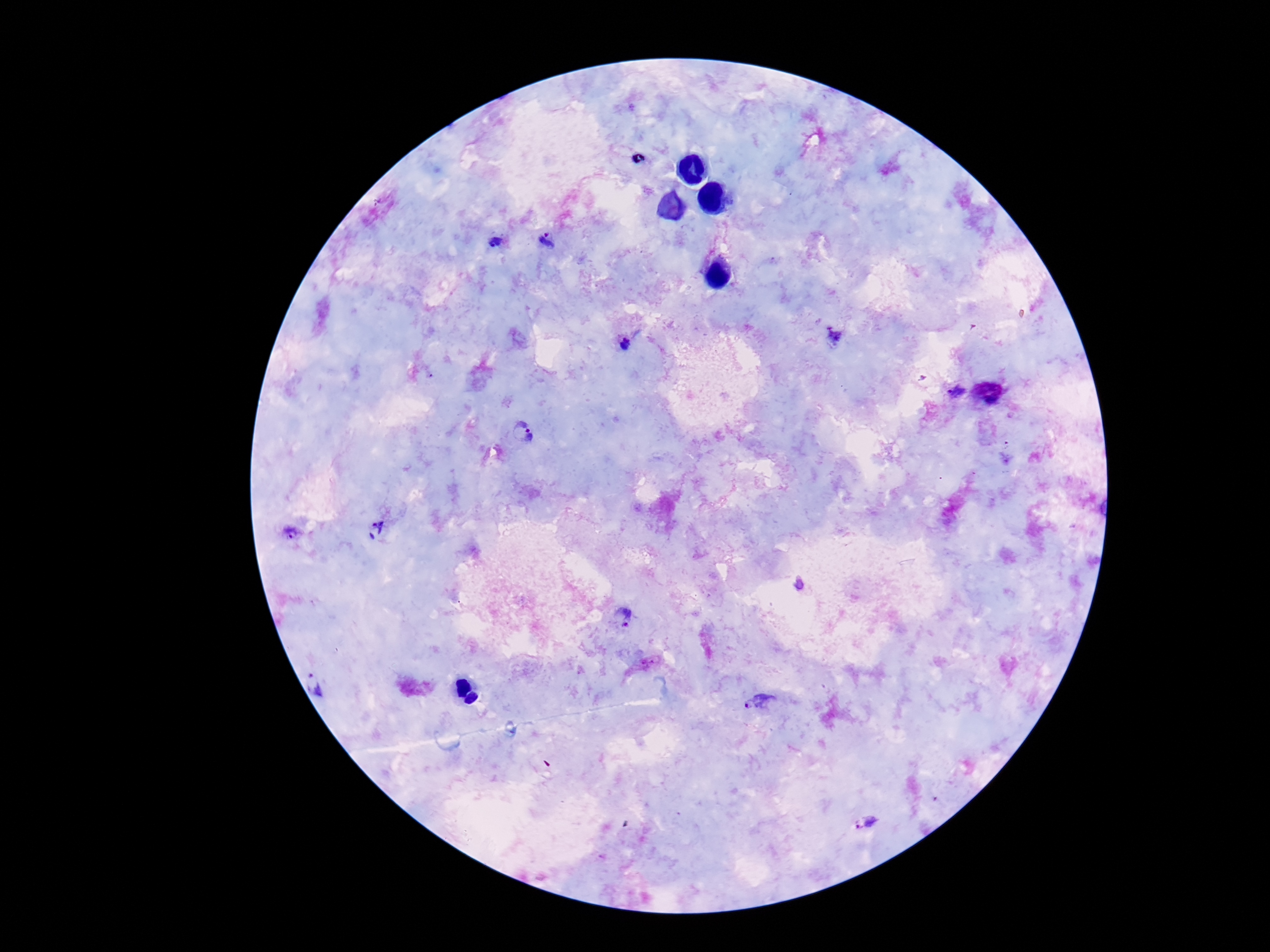
image size = 1270×952 pixels
magnification = 100x
stain = Giemsa
capture = smartphone camera through the microscope eyepiece
patient malaria status = positive
preparation = thick peripheral-blood smear
field of view = single
Plasmodium parasite locations = approximate centers as [x, y] in pixels: [546, 240], [496, 241], [832, 334], [625, 343], [956, 392], [520, 433], [378, 529], [292, 533], [623, 617], [318, 682], [760, 702], [865, 823]